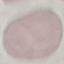
result = no malaria parasites detected
stain = Giemsa
image type = automatically extracted cell patch, resized to 64 × 64 pixels
preparation = thin smear
capture = smartphone through the microscope eyepiece